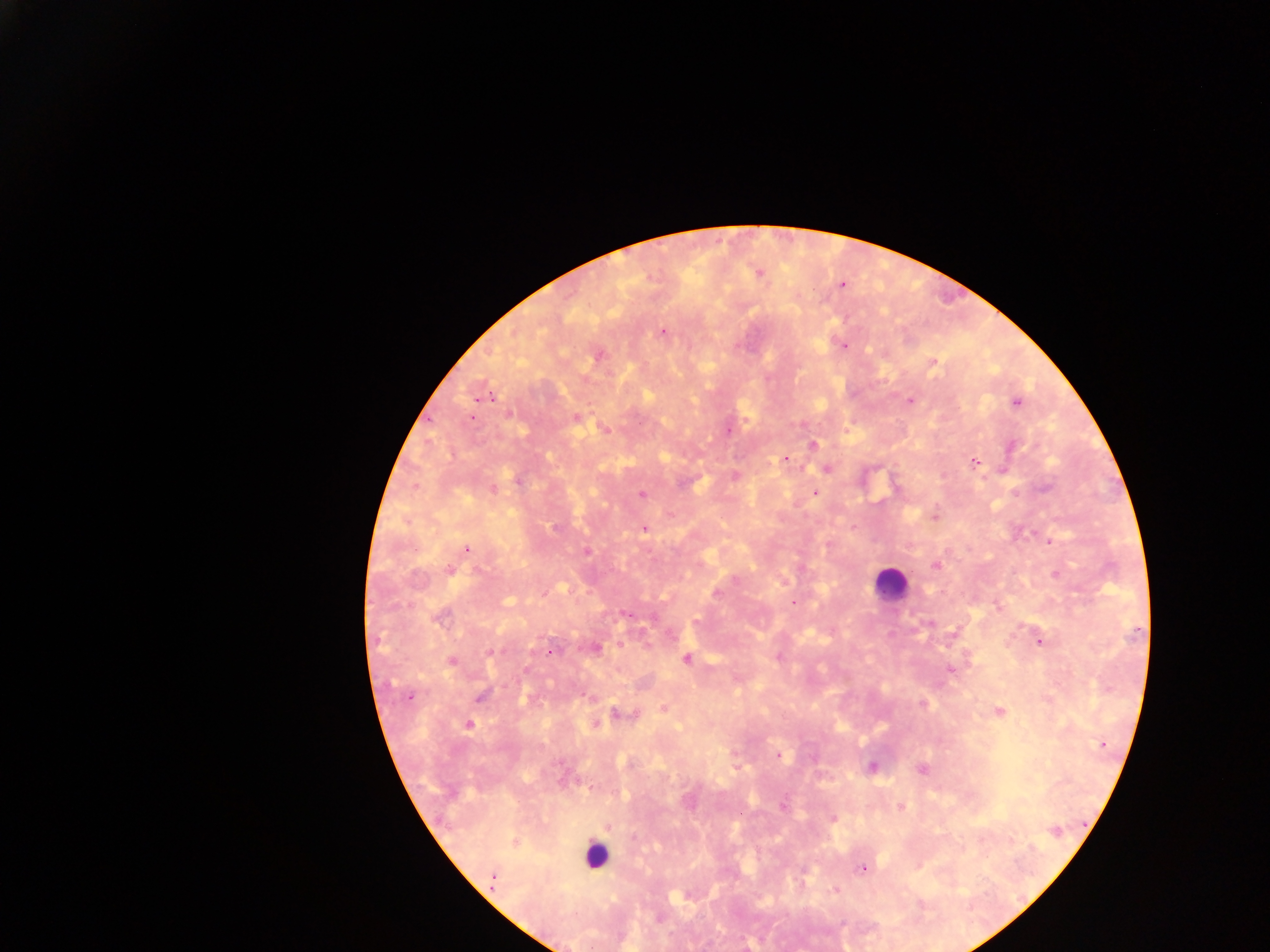
Approximate centers as x y in pixels. Malaria parasite locations: 759 274; 841 284; 662 332; 843 345; 598 355; 933 364; 485 397; 910 401; 1016 403; 471 418; 576 418; 605 429; 728 430; 812 445; 786 458; 974 462; 827 469; 735 476; 518 481; 1045 487; 492 490; 814 492; 641 494; 671 515; 934 515; 555 528; 644 529; 1051 542; 467 548; 587 552; 936 565; 450 570; 1056 574; 735 580; 717 595; 793 602; 627 613; 440 616; 696 622; 929 623; 1039 642; 597 647; 491 651; 551 652; 686 659; 451 661; 950 668; 410 696; 480 696; 923 704; 663 707; 999 712; 623 715; 469 725; 596 725; 1103 743; 779 755; 871 767; 922 769; 783 806; 901 808; 833 818; 608 826; 1055 831; 633 838; 515 843; 862 869; 493 880; 835 890. Leukocyte locations: 890 584; 595 855. Photographed through a microscope with a mobile-phone camera. Thick blood film. One field of view. Image is 1270×952 pixels. Collected in Ghana.